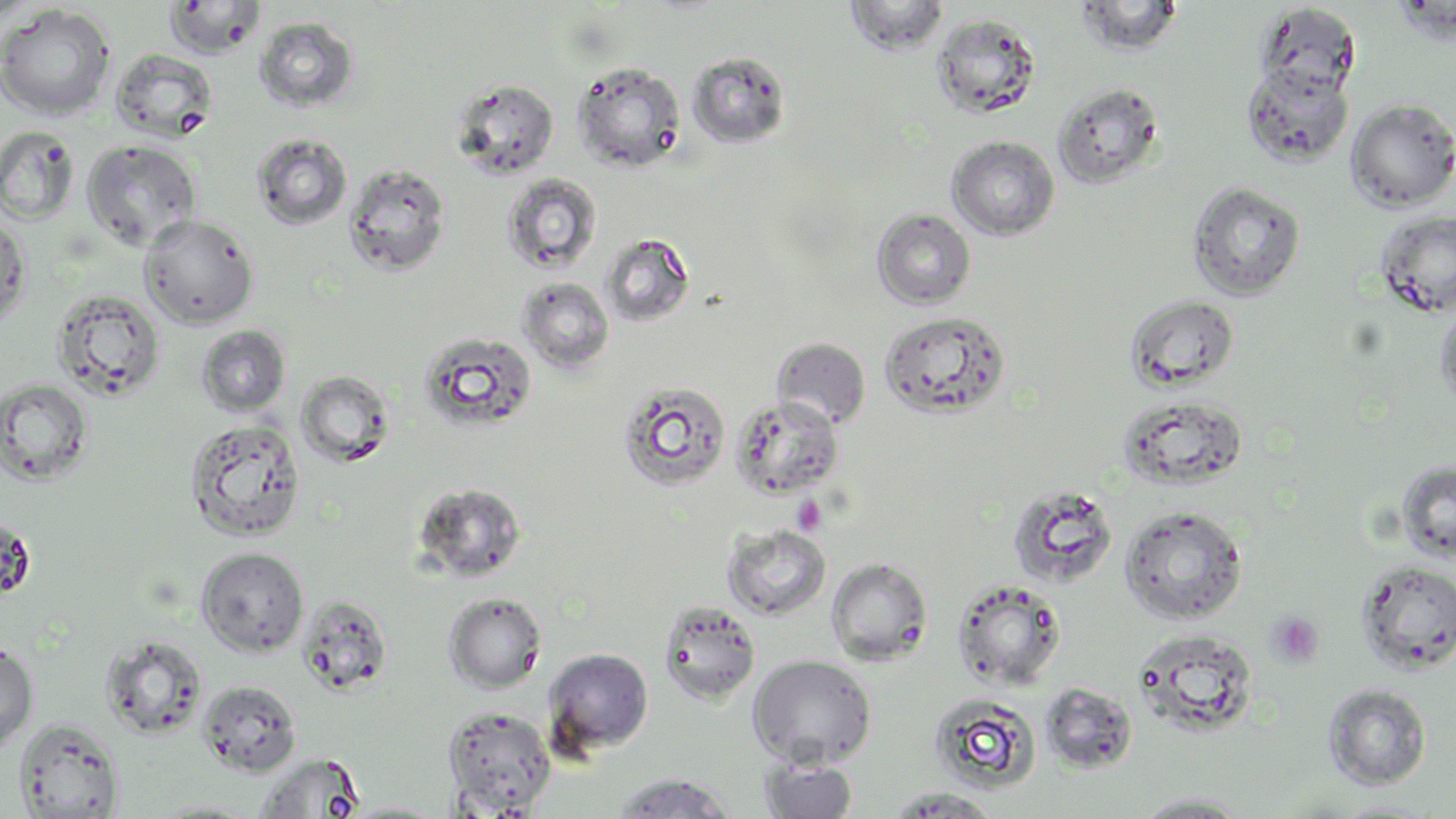

slide-level diagnosis = negative for blood parasites
image size = 1456×819 pixels
preparation = thin blood smear
uninfected red blood cell locations = approximate bounding boxes as (x1,y1)-(x2,y2) corner pairs in pixels: (163,0)-(267,58), (1073,0)-(1184,57), (844,1)-(949,55), (1254,3)-(1361,99), (0,4)-(116,121), (931,13)-(1040,118), (254,16)-(359,112), (110,48)-(219,141), (687,50)-(792,149), (572,60)-(686,174), (1242,63)-(1354,168), (449,77)-(560,180), (1052,82)-(1165,189), (1346,98)-(1456,211), (0,125)-(80,225), (250,132)-(354,231), (946,135)-(1060,241), (82,140)-(201,251), (343,162)-(451,277), (500,173)-(603,275), (1187,181)-(1305,301), (872,208)-(976,309), (0,211)-(31,329), (1375,211)-(1456,318), (139,214)-(259,328), (600,233)-(695,327), (517,276)-(614,374), (50,288)-(166,403), (1126,294)-(1240,391), (1434,303)-(1456,412), (879,310)-(1011,420), (195,324)-(291,417), (418,330)-(538,434), (772,337)-(871,430), (296,370)-(395,466), (1,377)-(93,486), (617,381)-(731,492), (1117,395)-(1249,491), (730,396)-(844,499), (185,418)-(307,541), (1396,460)-(1456,565), (412,481)-(528,581), (1006,484)-(1119,588), (1119,505)-(1249,624), (0,513)-(36,601), (722,524)-(832,620), (195,547)-(308,656), (826,557)-(933,666), (1355,559)-(1456,676), (952,578)-(1067,690), (444,592)-(547,693), (297,595)-(393,696), (658,599)-(761,705), (1131,628)-(1260,737), (100,634)-(207,739), (0,641)-(38,751), (543,648)-(654,755), (748,654)-(877,768), (197,680)-(301,776), (1040,682)-(1137,774), (1322,683)-(1432,790), (929,693)-(1042,794), (443,706)-(556,815), (14,718)-(124,818), (255,754)-(365,819), (760,758)-(859,818), (611,772)-(736,818), (883,787)-(1005,817), (1132,792)-(1255,817), (144,799)-(262,817), (1330,799)-(1443,818), (340,802)-(448,818)
modality = optical microscopy
field of view = single
magnification = 1000x
platelet locations = approximate bounding boxes as (x1,y1)-(x2,y2) corner pairs in pixels: (791,495)-(828,536), (1266,611)-(1325,667)
stain = May-Grünwald-Giemsa